Outline each blood parasite and name the species.
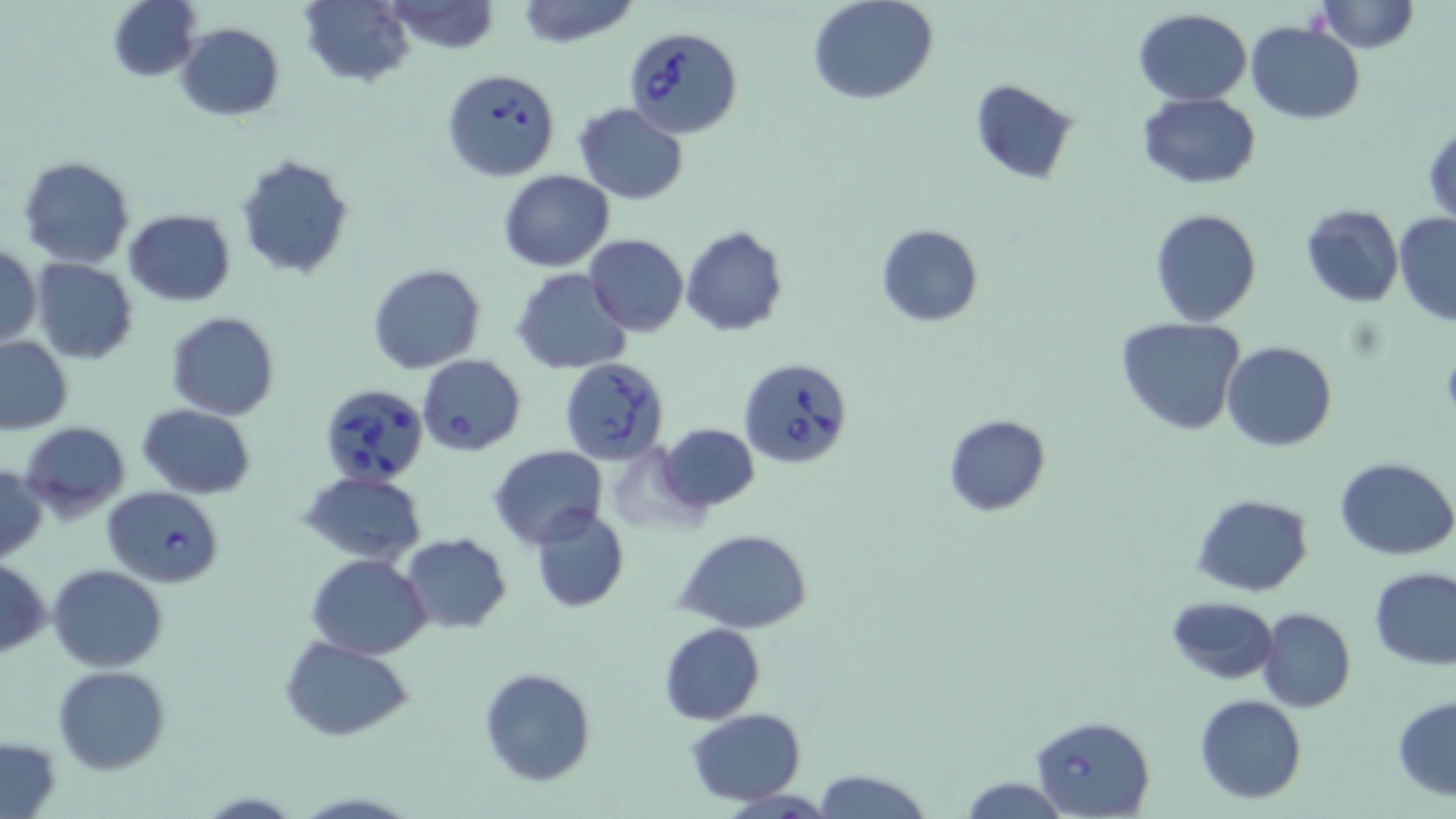
Approximate bounding boxes as (x1,y1)-(x2,y2) corner pairs in pixels.
Babesia divergens-infected red blood cells: (624,27)-(743,138), (442,69)-(558,181), (737,358)-(853,466), (558,359)-(669,464), (317,383)-(431,484), (104,487)-(224,587), (1031,715)-(1154,819).
No Plasmodium falciparum, Plasmodium ovale, Plasmodium malariae, Plasmodium vivax, or Trypanosoma brucei observed.

slide-level diagnosis = Babesia divergens
preparation = thin blood smear
stain = May-Grünwald-Giemsa
image size = 1456×819 pixels
modality = optical microscopy
field of view = one of a larger specimen
magnification = 1000x
uninfected red blood cell locations = approximate bounding boxes as (x1,y1)-(x2,y2) corner pairs in pixels: (107,0)-(201,81), (300,0)-(414,88), (514,0)-(642,48), (808,0)-(938,105), (1314,0)-(1420,53), (383,1)-(500,55), (1134,8)-(1251,106), (1248,21)-(1364,124), (176,23)-(284,120), (969,78)-(1081,184), (1138,92)-(1261,188), (572,104)-(688,203), (1425,122)-(1455,226), (235,154)-(356,281), (18,157)-(134,269), (498,169)-(614,271), (1300,204)-(1404,307), (1150,209)-(1261,327), (123,210)-(235,306), (1394,213)-(1456,326), (876,224)-(984,327), (680,227)-(787,336), (584,234)-(688,337), (1,244)-(41,348), (30,258)-(138,363), (369,263)-(486,374), (513,269)-(634,375), (167,312)-(278,420), (1115,317)-(1246,435), (0,336)-(74,435), (1222,342)-(1336,451), (417,354)-(526,456), (137,405)-(257,498), (942,413)-(1051,514), (20,420)-(131,518), (657,422)-(760,512), (489,445)-(606,548), (1335,457)-(1455,559), (0,463)-(45,563), (300,470)-(429,563), (1191,494)-(1313,597), (530,506)-(629,614), (678,530)-(813,634), (400,533)-(513,634), (306,555)-(432,659), (0,560)-(49,656), (49,564)-(166,671), (1369,566)-(1456,669), (1167,597)-(1279,684), (1257,607)-(1354,713), (659,623)-(766,725), (283,637)-(412,740), (52,665)-(170,775), (478,667)-(596,787), (1194,694)-(1307,804), (1393,696)-(1456,799), (685,708)-(807,805), (1,735)-(62,816), (813,767)-(930,819), (957,776)-(1069,817)